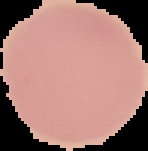

{
  "preparation": "thin blood film",
  "malaria_status": "uninfected",
  "image_type": "segmented cell region on a black background",
  "image_size": "148×151 pixels"
}